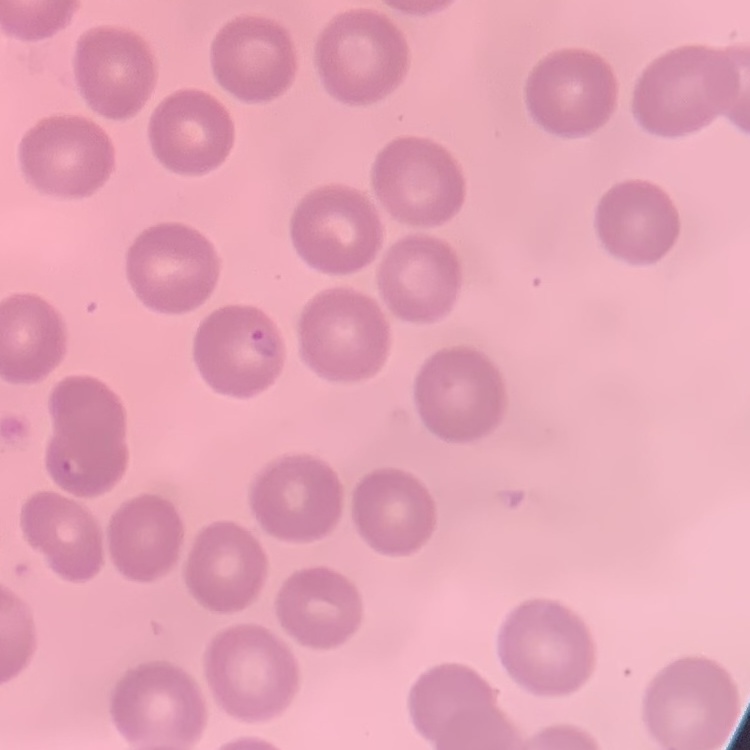

The red blood cells show no rouleaux formation. Square crop of a larger photomicrograph. Thin blood film. Stained with either Field's or Giemsa.